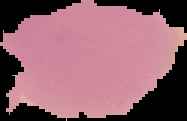

{
  "image_type": "segmented cell region with the area outside set to black",
  "preparation": "thin blood smear",
  "malaria_status": "uninfected",
  "image_size": "187×121 pixels"
}